Assess this cell for malaria.
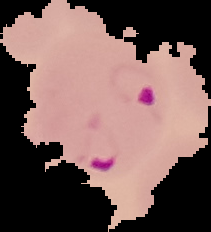
Parasitized.

Summary:
  - Image type: segmented cell region on a black background
  - Image size: 211×232 pixels
  - Preparation: thin blood smear